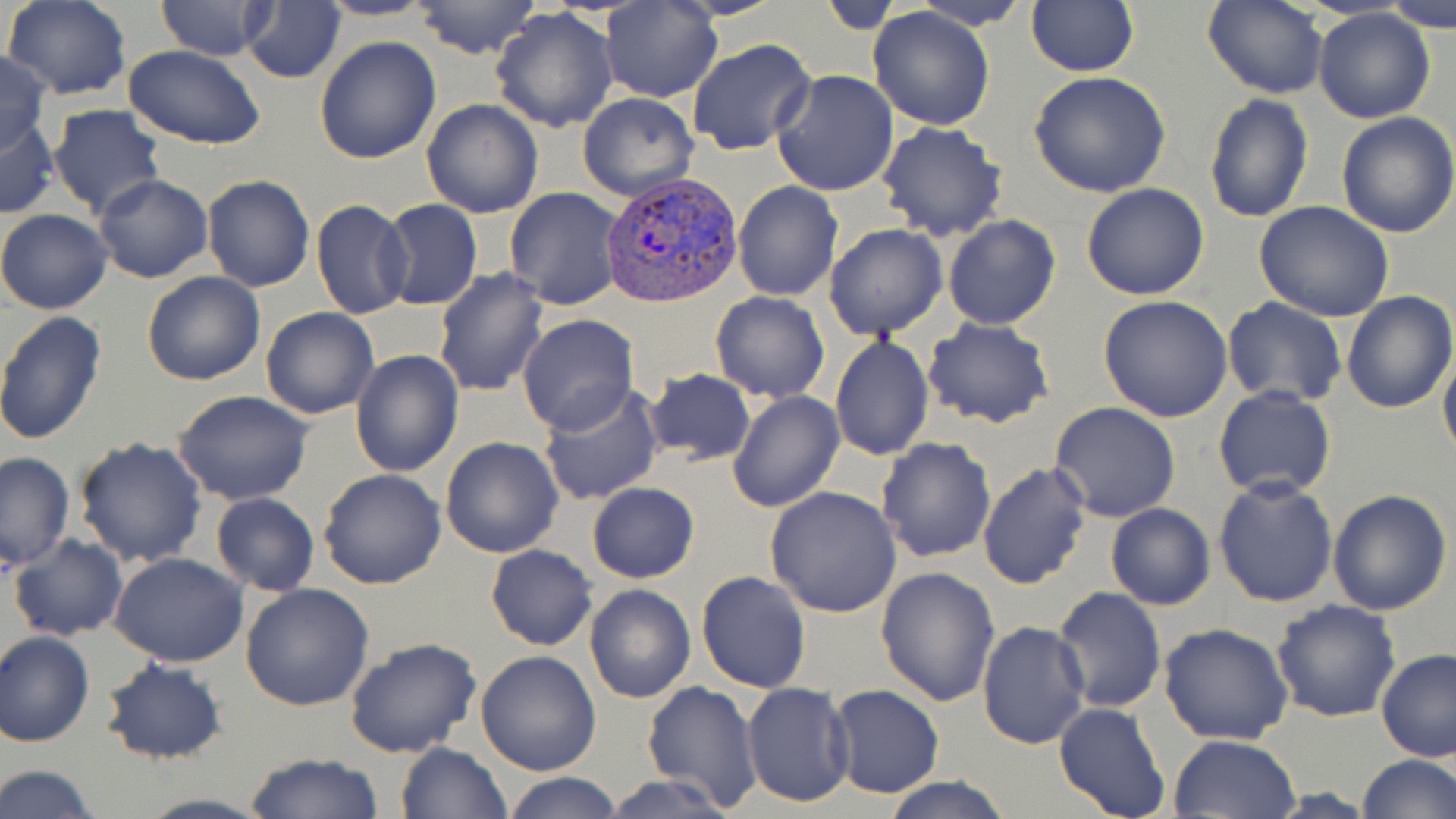
Plasmodium vivax-infected red blood cell locations = approximate bounding boxes as (x1,y1)-(x2,y2) corner pairs in pixels: (602,173)-(740,307)
slide-level diagnosis = Plasmodium vivax
image size = 1456×819 pixels
preparation = thin blood film
field of view = single
modality = light microscopy
stain = May-Grünwald-Giemsa
magnification = 1000x
uninfected red blood cell locations = approximate bounding boxes as (x1,y1)-(x2,y2) corner pairs in pixels: (3,0)-(131,99), (241,0)-(347,85), (315,0)-(440,21), (409,0)-(542,60), (156,1)-(275,58), (601,1)-(722,102), (906,1)-(1036,30), (1026,1)-(1140,76), (1202,1)-(1328,100), (1384,1)-(1456,30), (868,6)-(996,131), (490,7)-(620,134), (1314,8)-(1436,125), (314,36)-(441,164), (686,37)-(817,157), (123,46)-(267,147), (0,50)-(53,156), (769,69)-(898,196), (1028,71)-(1173,196), (577,92)-(701,203), (1204,94)-(1314,223), (421,98)-(545,220), (46,104)-(165,221), (1335,112)-(1456,239), (1,115)-(60,221), (875,122)-(1009,242), (94,174)-(213,284), (203,174)-(315,292), (733,182)-(842,301), (1081,183)-(1210,300), (504,186)-(626,310), (376,198)-(484,312), (311,199)-(413,321), (1252,200)-(1395,321), (0,209)-(112,315), (941,214)-(1063,330), (823,223)-(948,339), (433,270)-(549,397), (142,271)-(267,386), (1340,290)-(1455,413), (710,291)-(831,403), (1099,295)-(1235,422), (1221,297)-(1347,405), (260,306)-(378,419), (0,311)-(108,447), (516,314)-(638,437), (924,317)-(1056,428), (829,335)-(934,461), (1439,344)-(1456,464), (350,350)-(464,478), (644,367)-(757,466), (539,385)-(665,505), (1213,385)-(1336,500), (726,389)-(847,512), (170,390)-(316,507), (1049,402)-(1181,523), (440,436)-(565,557), (876,436)-(998,562), (73,437)-(208,570), (0,452)-(74,572), (976,461)-(1091,590), (319,468)-(448,589), (1212,477)-(1340,608), (585,482)-(699,582), (766,485)-(901,617), (1328,488)-(1452,615), (211,492)-(320,596), (1105,503)-(1216,610), (8,532)-(127,642), (485,545)-(597,650), (109,552)-(249,669), (875,566)-(1003,707), (695,569)-(812,694), (240,583)-(375,712), (584,583)-(696,704), (1052,586)-(1166,714), (1270,599)-(1401,722), (976,622)-(1089,750), (1157,623)-(1293,745), (1,630)-(96,747), (343,637)-(482,758), (1375,648)-(1456,762), (475,650)-(602,776), (100,658)-(228,765), (641,681)-(762,811), (741,682)-(855,807), (827,685)-(945,798), (1053,701)-(1171,819), (1167,733)-(1301,818), (395,742)-(511,818), (244,751)-(384,819), (1356,754)-(1456,819), (1,763)-(98,819), (503,773)-(622,819), (600,773)-(743,819), (880,777)-(1015,818), (131,793)-(273,819)